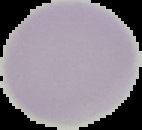
Summary:
  - Image type: segmented cell region with the area outside set to black
  - Image size: 142×130 pixels
  - Malaria status: uninfected
  - Preparation: thin blood smear